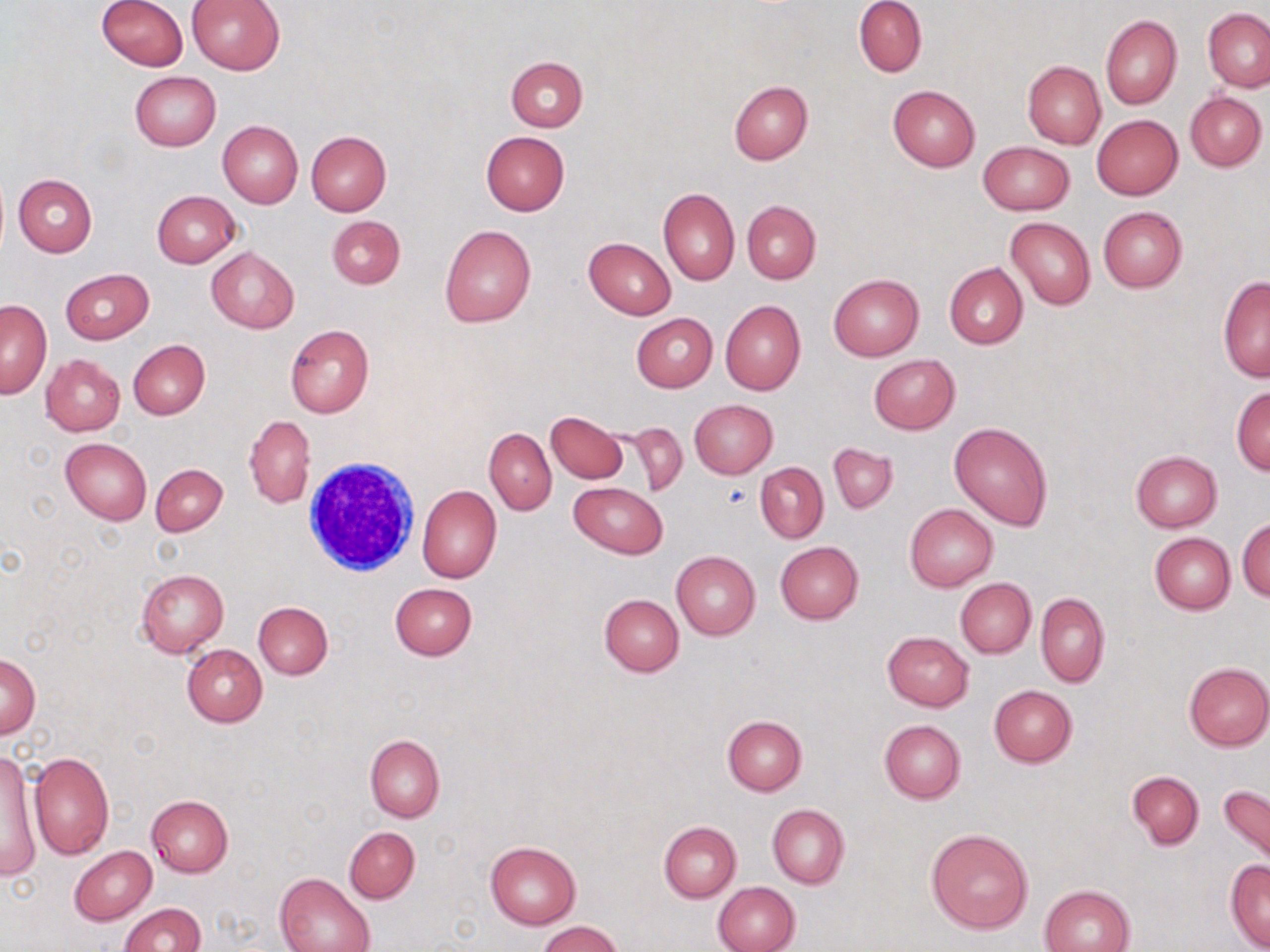
slide-level diagnosis = no evidence of blood parasites
preparation = thin blood smear
white blood cell locations = approximate bounding boxes as (x1, y1, x2, y2) in pixels: (303, 454, 423, 578)
field of view = one of a larger specimen
magnification = 1000x
modality = optical microscopy
uninfected red blood cell locations = approximate bounding boxes as (x1, y1, x2, y2) in pixels: (95, 0, 187, 71), (185, 0, 286, 75), (855, 0, 927, 77), (1204, 8, 1270, 92), (1100, 15, 1181, 110), (505, 55, 587, 131), (1022, 61, 1106, 149), (130, 71, 221, 151), (728, 81, 812, 165), (887, 84, 980, 171), (1185, 91, 1267, 170), (1091, 114, 1183, 200), (217, 120, 302, 206), (306, 131, 391, 215), (480, 131, 570, 215), (978, 141, 1075, 215), (13, 174, 98, 256), (658, 188, 740, 285), (151, 190, 240, 268), (742, 200, 821, 284), (1098, 206, 1188, 293), (327, 215, 405, 288), (1006, 216, 1095, 310), (440, 225, 536, 328), (583, 237, 677, 319), (206, 247, 299, 333), (944, 262, 1028, 349), (60, 268, 153, 344), (828, 274, 924, 360), (1218, 277, 1269, 381), (720, 300, 806, 395), (0, 301, 51, 399), (630, 313, 718, 391), (286, 324, 374, 418), (128, 340, 209, 419), (41, 354, 125, 436), (869, 354, 960, 434), (1232, 384, 1270, 475), (689, 399, 778, 479), (546, 410, 628, 483), (245, 415, 315, 509), (624, 422, 687, 498), (949, 422, 1053, 530), (484, 429, 555, 515), (61, 438, 152, 524), (827, 442, 898, 514), (1130, 450, 1222, 532), (755, 463, 828, 541), (151, 464, 227, 536), (569, 482, 668, 559), (417, 485, 501, 584), (905, 502, 998, 592), (1237, 518, 1270, 602), (1149, 532, 1235, 613), (775, 542, 863, 624), (672, 551, 761, 640), (137, 568, 230, 657), (955, 578, 1036, 659), (388, 583, 476, 660), (1036, 591, 1110, 687), (598, 593, 683, 677), (253, 601, 332, 679), (882, 631, 974, 711), (182, 645, 268, 726), (1, 653, 40, 738), (1182, 662, 1270, 751), (989, 685, 1077, 767), (723, 716, 807, 795), (878, 719, 966, 803), (365, 735, 445, 823), (2, 748, 43, 881), (28, 752, 114, 858), (1127, 771, 1204, 849), (1217, 784, 1270, 869), (145, 795, 233, 877), (767, 804, 848, 889), (659, 821, 741, 902), (344, 826, 420, 904), (926, 828, 1034, 934), (485, 840, 582, 928), (70, 846, 157, 925), (1225, 860, 1270, 951), (275, 872, 375, 952), (711, 882, 800, 951), (1038, 885, 1135, 952), (120, 903, 206, 951), (537, 920, 625, 952)
image size = 1270×952 pixels
stain = May-Grünwald-Giemsa
platelet locations = approximate bounding boxes as (x1, y1, x2, y2) in pixels: (722, 484, 751, 509)